Report the malaria status of this cell.
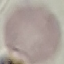
It is uninfected.

preparation: thin blood smear
capture: smartphone camera at the microscope eyepiece
image_type: automatically extracted cell patch, resized to 64 × 64 pixels
stain: Giemsa